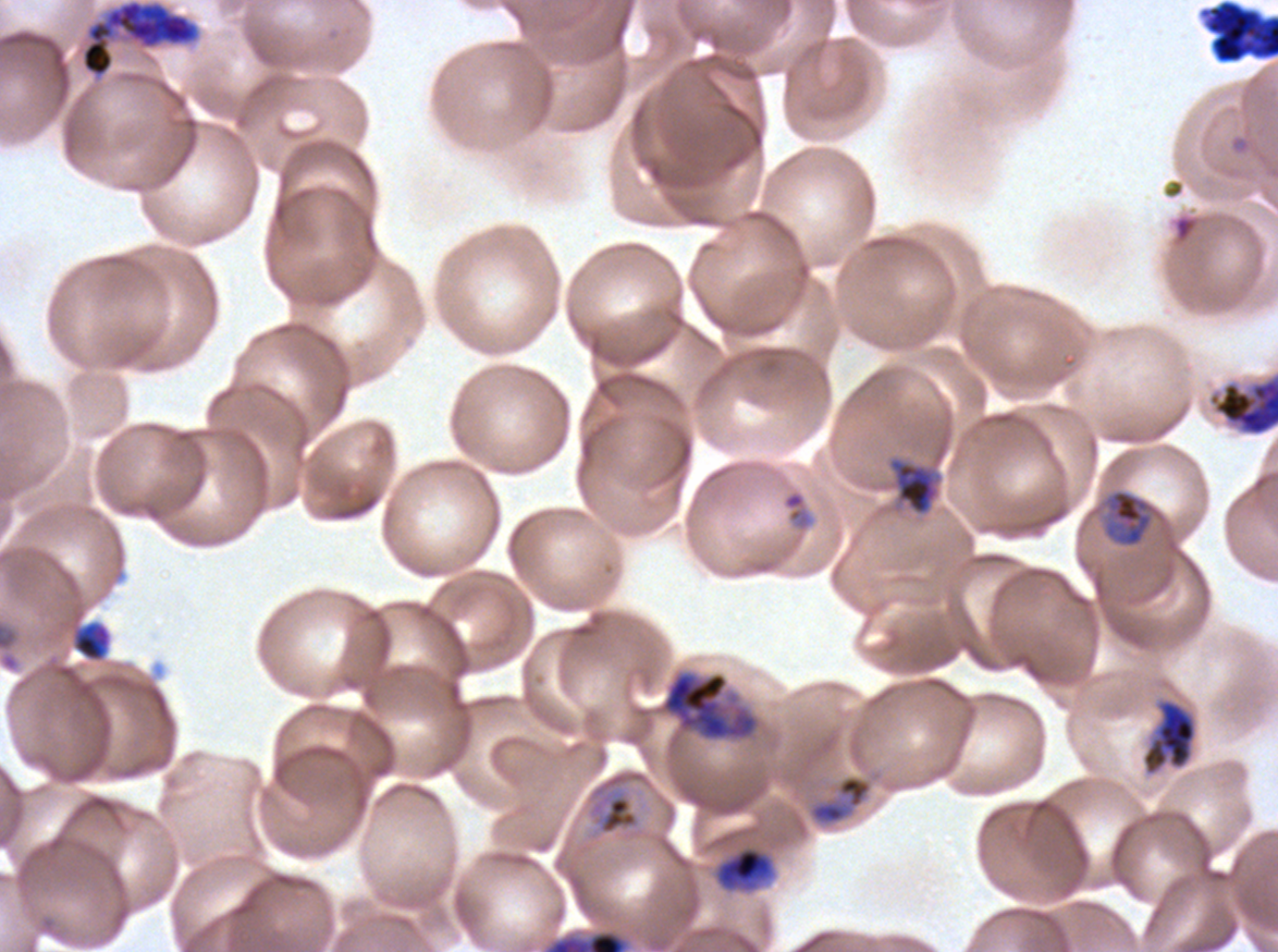

Approximate bounding boxes as {x1, y1, x2, y2} in pixels. Late schizont locations: {542, 928, 632, 951}. Mid trophozoite locations: {1103, 489, 1155, 548}, {596, 794, 639, 836}, {712, 844, 777, 894}. Early schizont locations: {80, 0, 200, 79}, {886, 455, 944, 517}, {653, 669, 761, 743}. Late trophozoite locations: {1141, 699, 1197, 775}. Debris locations: {1198, 0, 1277, 64}, {74, 624, 110, 661}, {809, 775, 873, 825}. Ring locations: {1235, 137, 1249, 152}, {780, 487, 817, 549}. Life-cycle stages observed: ring, mid trophozoite, late trophozoite, early schizont, late schizont. A sub-image separated from a larger composite. Thin blood film. Image is 1278×952 pixels. Ex-vivo Plasmodium falciparum culture from a patient in The Gambia, grown for 24 to 48 hours. Giemsa stain.